Identify the blood parasite species.
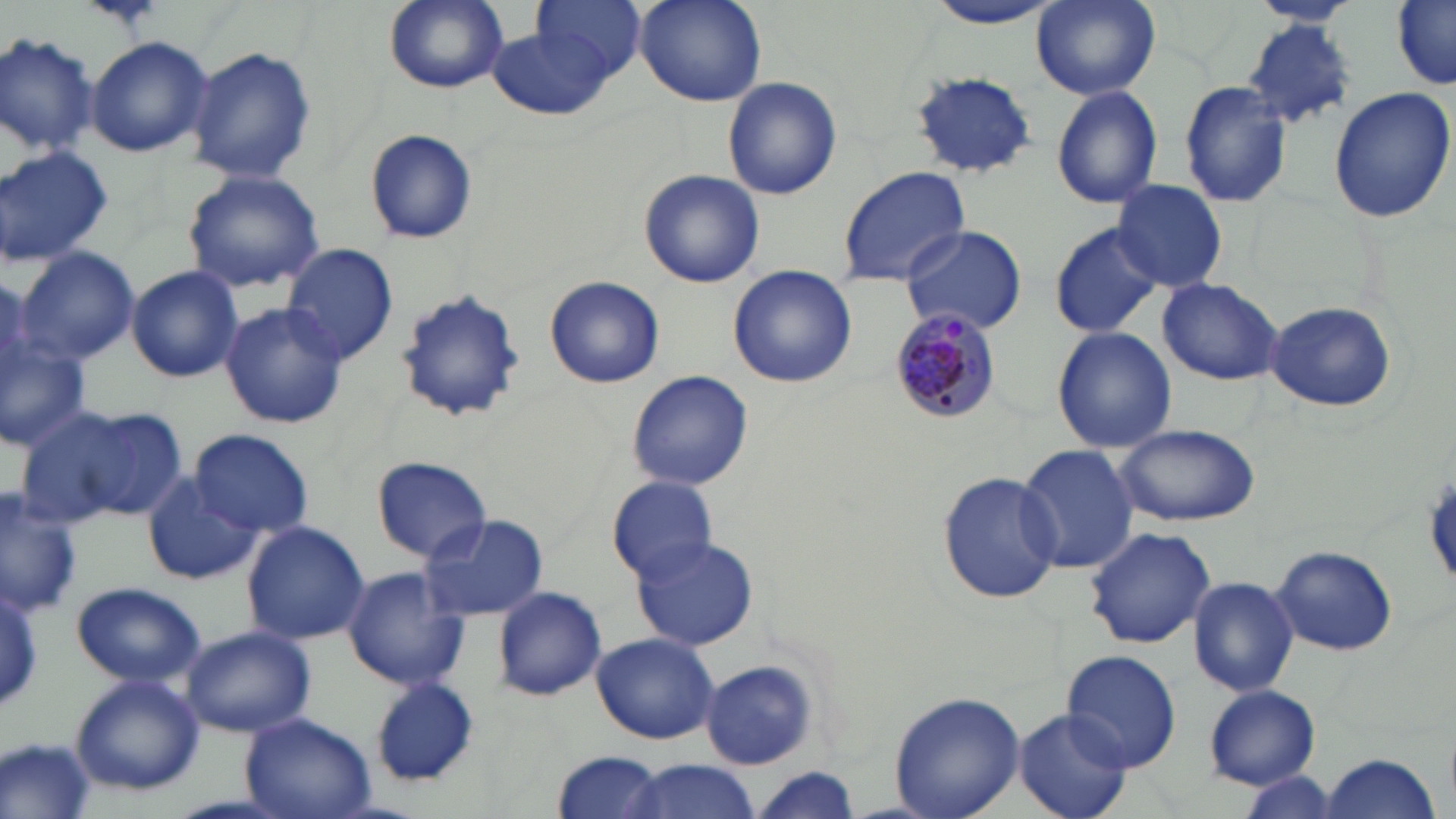

Plasmodium malariae.

Summary:
  - Coordinate format: approximate bounding boxes as (x1, y1, x2, y2) in pixels
  - Plasmodium malariae-infected red blood cell locations: (886, 306, 1001, 426)
  - Uninfected red blood cell locations: (382, 0, 508, 93), (535, 0, 647, 82), (634, 0, 765, 106), (927, 0, 1061, 30), (1247, 0, 1361, 31), (1031, 1, 1161, 100), (1393, 2, 1455, 87), (1243, 19, 1356, 126), (488, 27, 615, 121), (0, 32, 98, 157), (85, 35, 213, 158), (186, 46, 318, 184), (909, 70, 1039, 179), (722, 77, 843, 200), (1179, 80, 1292, 210), (1050, 86, 1164, 209), (1327, 87, 1454, 223), (365, 129, 479, 242), (0, 145, 113, 265), (837, 166, 969, 286), (639, 168, 765, 288), (181, 169, 325, 294), (1111, 179, 1230, 293), (1048, 220, 1165, 339), (900, 225, 1026, 334), (282, 244, 399, 363), (15, 246, 140, 366), (126, 264, 244, 384), (728, 264, 857, 388), (546, 276, 665, 387), (1158, 278, 1283, 385), (394, 288, 525, 426), (1265, 301, 1398, 414), (219, 302, 349, 428), (1052, 325, 1176, 454), (0, 330, 91, 454), (627, 369, 753, 491), (14, 401, 180, 530), (1112, 424, 1259, 525), (183, 429, 315, 539), (1015, 444, 1139, 576), (372, 455, 492, 563), (936, 469, 1063, 607), (141, 472, 263, 586), (609, 476, 720, 584), (0, 489, 84, 618), (418, 512, 549, 622), (241, 521, 370, 645), (1084, 526, 1216, 648), (631, 536, 760, 653), (1272, 547, 1396, 656), (340, 567, 470, 692), (1188, 576, 1299, 697), (71, 580, 205, 688), (491, 585, 607, 702), (0, 586, 45, 705), (181, 625, 316, 738), (592, 632, 718, 745), (1062, 651, 1181, 771), (700, 660, 819, 771), (69, 673, 205, 795), (368, 678, 479, 787), (1204, 686, 1321, 789), (887, 691, 1025, 819), (1016, 709, 1134, 819), (241, 712, 376, 819), (2, 736, 96, 819), (549, 751, 669, 819), (1321, 753, 1440, 819), (615, 758, 764, 819), (750, 766, 865, 819), (1236, 771, 1345, 817)
  - Stain: May-Grünwald-Giemsa
  - Image size: 1456×819 pixels
  - Magnification: 1000x
  - Preparation: thin blood film
  - Field of view: single
  - Modality: optical microscopy